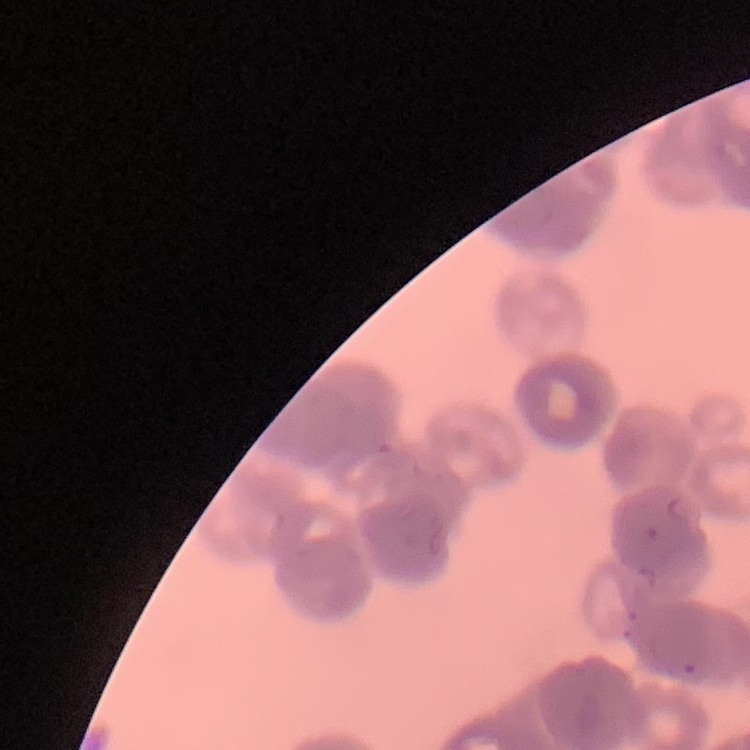

{
  "red_blood_cell_morphology": "rouleaux formation",
  "stain": "Field's or Giemsa",
  "image_type": "one tile cut from a larger photomicrograph",
  "preparation": "thin peripheral smear"
}